Assess this cell for malaria.
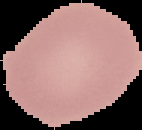
It is uninfected.

image type = segmented cell region on a black background
preparation = thin blood smear
image size = 142×130 pixels